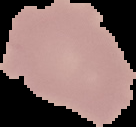
malaria status = uninfected
image type = cell region segmented out of the field of view; surrounding area masked to black
preparation = thin blood smear
image size = 136×127 pixels